Identify the blood parasite species.
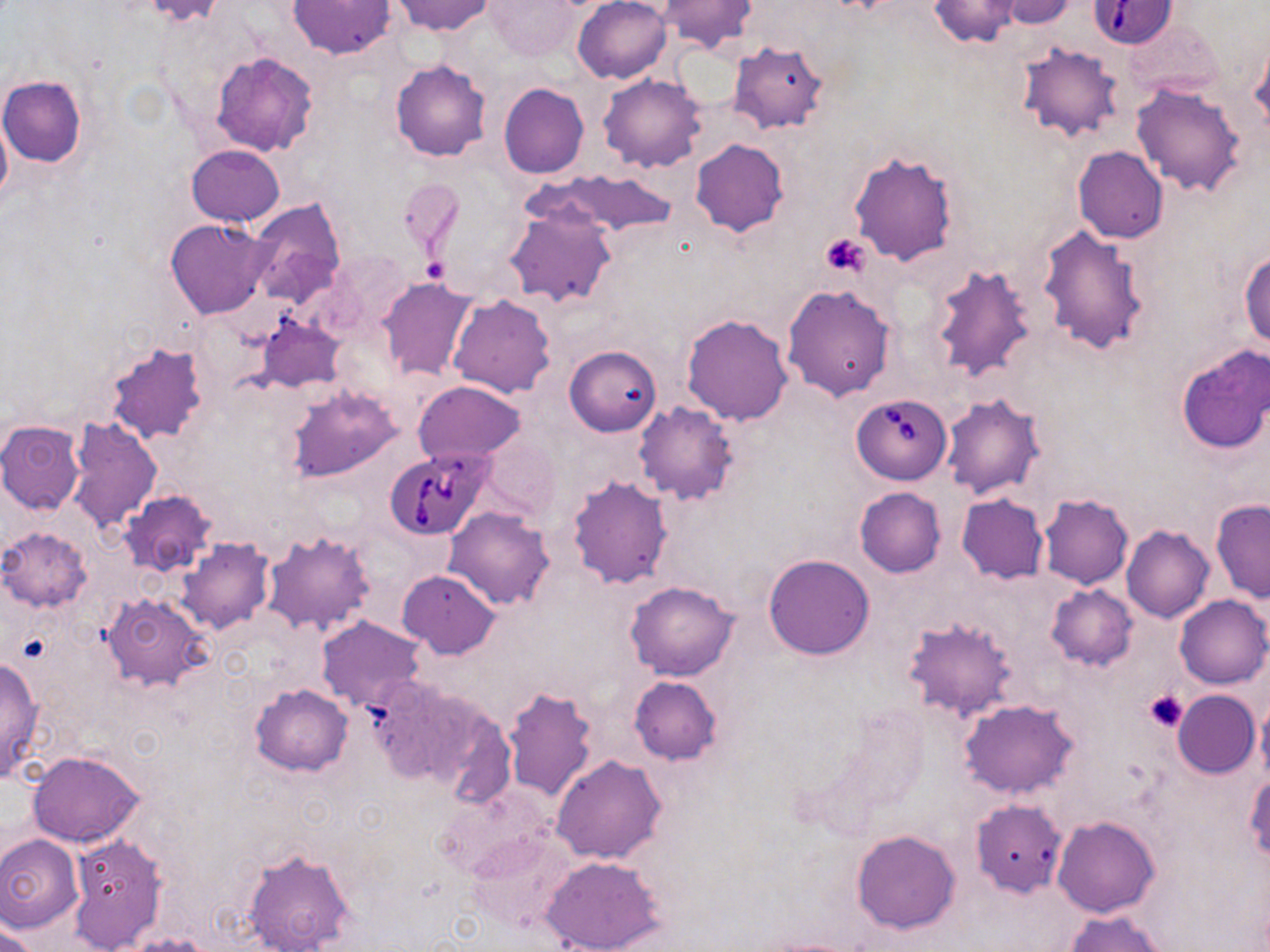

Babesia divergens.

Approximate bounding boxes as (x1,y1)-(x2,y2) corner pairs in pixels. Uninfected red blood cell locations: (289,0)-(393,58), (391,0)-(494,36), (572,0)-(672,84), (930,0)-(1021,47), (996,0)-(1078,28), (485,1)-(580,61), (656,1)-(757,55), (728,41)-(830,135), (1017,42)-(1122,143), (1249,43)-(1269,137), (210,52)-(319,157), (390,59)-(491,161), (598,73)-(708,172), (0,76)-(86,167), (1130,82)-(1248,197), (499,83)-(588,179), (0,110)-(12,209), (690,138)-(789,237), (185,145)-(285,227), (1073,146)-(1168,244), (849,151)-(959,267), (543,169)-(678,239), (397,177)-(464,261), (246,199)-(346,309), (503,201)-(617,311), (166,218)-(272,319), (1037,225)-(1151,355), (1240,249)-(1270,349), (929,265)-(1038,384), (377,276)-(479,383), (782,284)-(895,400), (448,293)-(555,397), (256,314)-(345,392), (682,314)-(793,426), (104,340)-(209,444), (566,345)-(662,436), (1175,345)-(1270,454), (413,380)-(526,465), (285,385)-(402,483), (940,393)-(1046,500), (633,401)-(740,506), (67,416)-(162,535), (0,419)-(86,515), (481,432)-(559,521), (567,474)-(675,590), (855,488)-(946,577), (117,490)-(218,577), (957,494)-(1049,584), (1039,494)-(1133,590), (1211,498)-(1270,603), (443,506)-(557,611), (1121,525)-(1215,624), (1,528)-(91,611), (260,529)-(376,637), (178,538)-(273,633), (764,554)-(874,660), (397,569)-(501,659), (626,581)-(739,681), (1045,584)-(1138,672), (101,593)-(211,693), (1174,594)-(1269,689), (315,615)-(426,713), (902,618)-(1017,721), (0,656)-(46,783), (362,674)-(501,795), (629,675)-(722,764), (249,683)-(353,776), (501,687)-(600,804), (1172,690)-(1259,779), (1255,692)-(1270,788), (959,698)-(1081,799), (27,750)-(144,848), (550,754)-(668,865), (1244,773)-(1270,861), (969,798)-(1068,897), (1052,815)-(1160,918), (467,827)-(578,933), (852,830)-(962,934), (0,833)-(85,932), (68,834)-(167,951), (241,845)-(356,951), (539,855)-(665,952), (1063,910)-(1168,952), (0,918)-(44,951), (123,934)-(215,952). Babesia divergens-infected red blood cell locations: (1089,2)-(1180,49), (852,392)-(950,484), (382,447)-(492,540). Platelet locations: (821,232)-(870,276), (419,258)-(447,285), (1144,689)-(1188,732). May-Grünwald-Giemsa stain. Thin blood film. Single field of view. Image is 1270×952 pixels. 1000x magnification. Light microscopy.